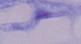

A trypanosome is shown. Captured at 1000x magnification. Photomicrograph.